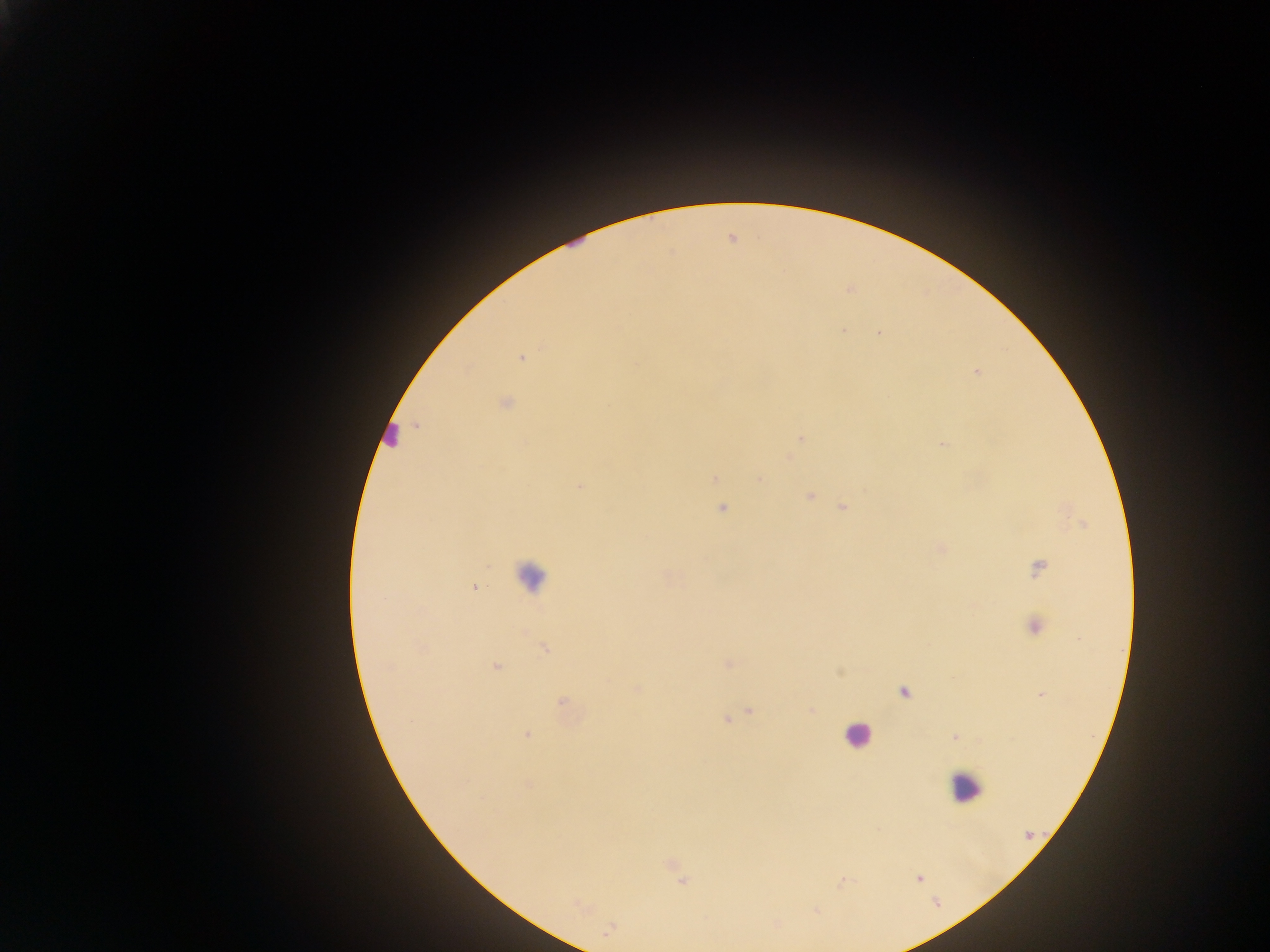
capture = mobile-phone photograph through a microscope
image size = 1270×952 pixels
Plasmodium parasite locations = approximate centers as {x, y} in pixels: {522, 358}, {977, 372}, {505, 403}, {417, 426}, {801, 438}, {943, 444}, {715, 479}, {580, 486}, {810, 496}, {843, 507}, {722, 509}, {1038, 568}, {474, 588}, {1034, 627}, {545, 649}, {496, 667}, {903, 692}, {1042, 695}, {562, 702}, {750, 711}, {727, 719}, {527, 734}, {955, 737}, {528, 785}, {919, 879}
country = Ghana
leukocyte locations = approximate centers as {x, y} in pixels: {389, 432}, {530, 575}, {857, 735}, {965, 786}
field of view = single
preparation = thick blood smear